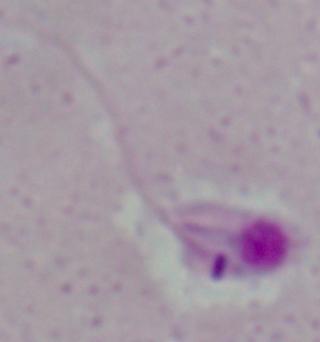

magnification = 1000x
modality = micrograph
identification = Leishmania